Classify this cell by malaria status.
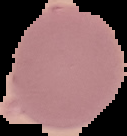

It is uninfected.

image size = 127×136 pixels
image type = segmented cell region on a black background
preparation = thin blood smear